Assess for Plasmodium parasites.
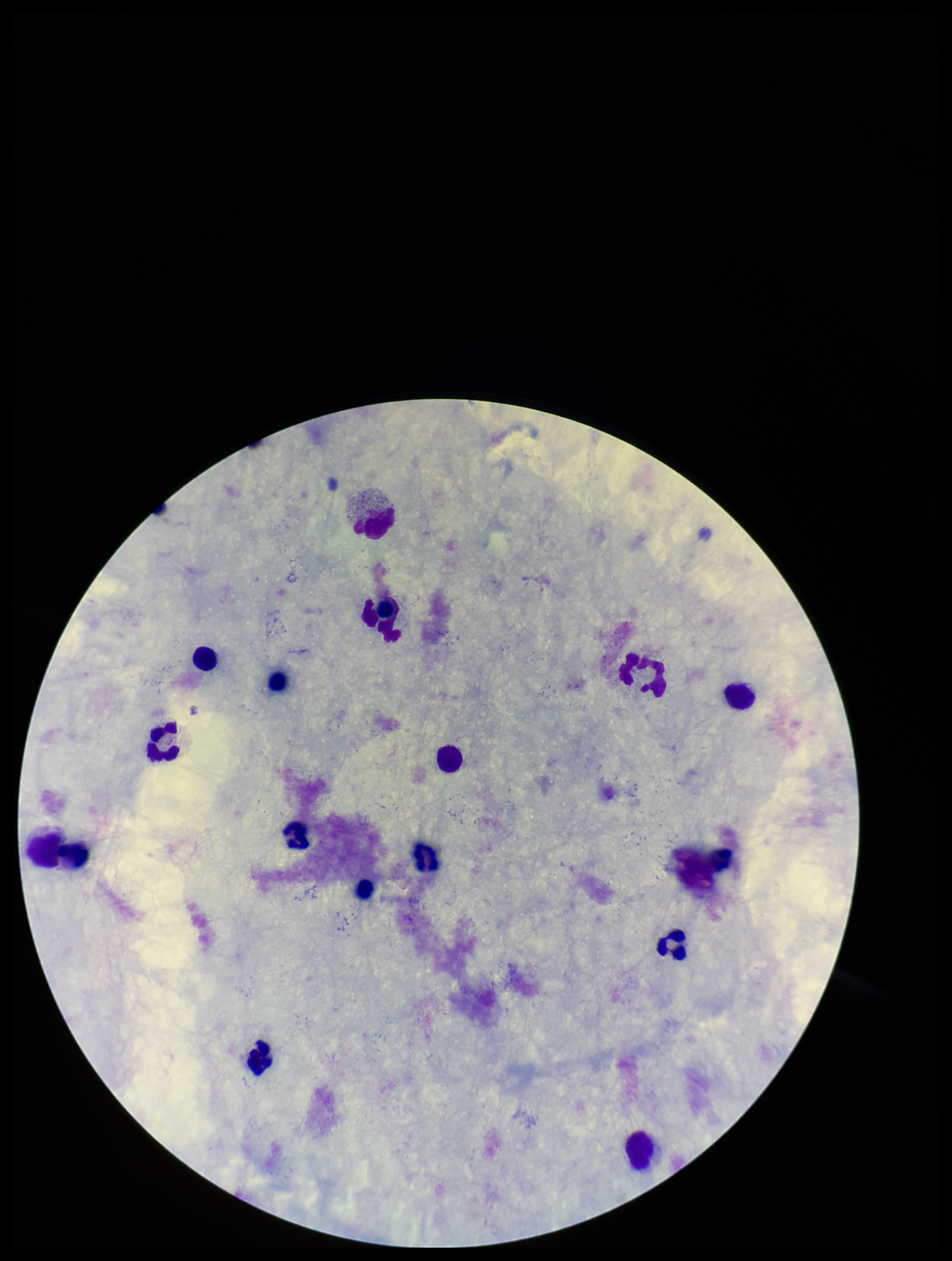

None seen.

Summary:
  - Patient malaria status: negative
  - Leukocyte count: 15
  - Stain: Giemsa
  - Capture: smartphone photograph through the microscope eyepiece
  - Field of view: single
  - Parasite count: 0
  - Preparation: thick
  - Image size: 952×1261 pixels